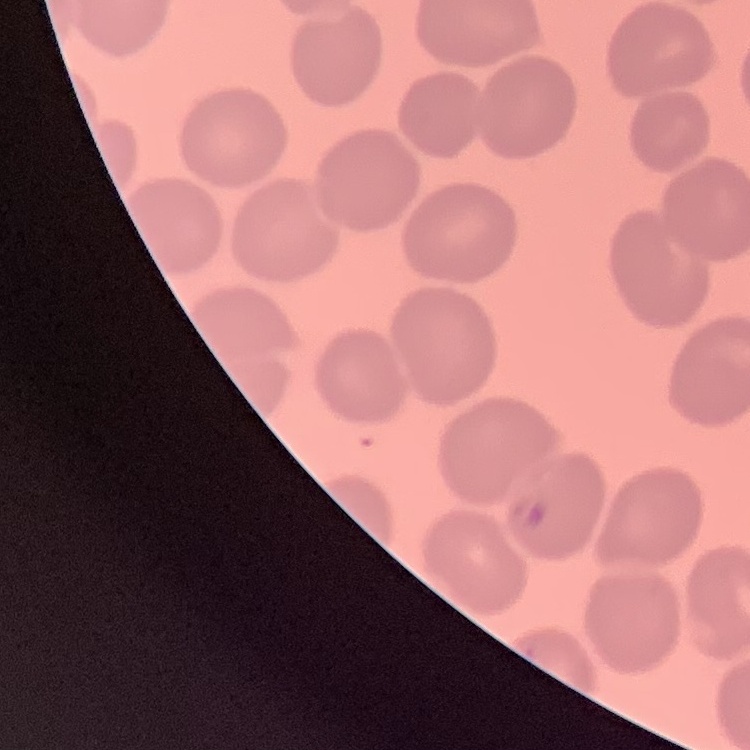 The red blood cells exhibit no rouleaux formation. One tile cut from a larger photomicrograph. Thin peripheral smear. Field's or Giemsa stain.